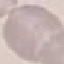

result = negative for malaria parasites
capture = smartphone through the microscope eyepiece
preparation = thin blood smear
image type = automatically extracted cell patch, resized to 64 × 64 pixels
stain = Giemsa